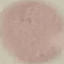

Result: no malaria parasites detected. Acquired by smartphone through the microscope eyepiece. Automatically extracted cell patch, resized to 64 × 64 pixels. Thin blood film. Giemsa stain.